Locate and identify every blood parasite.
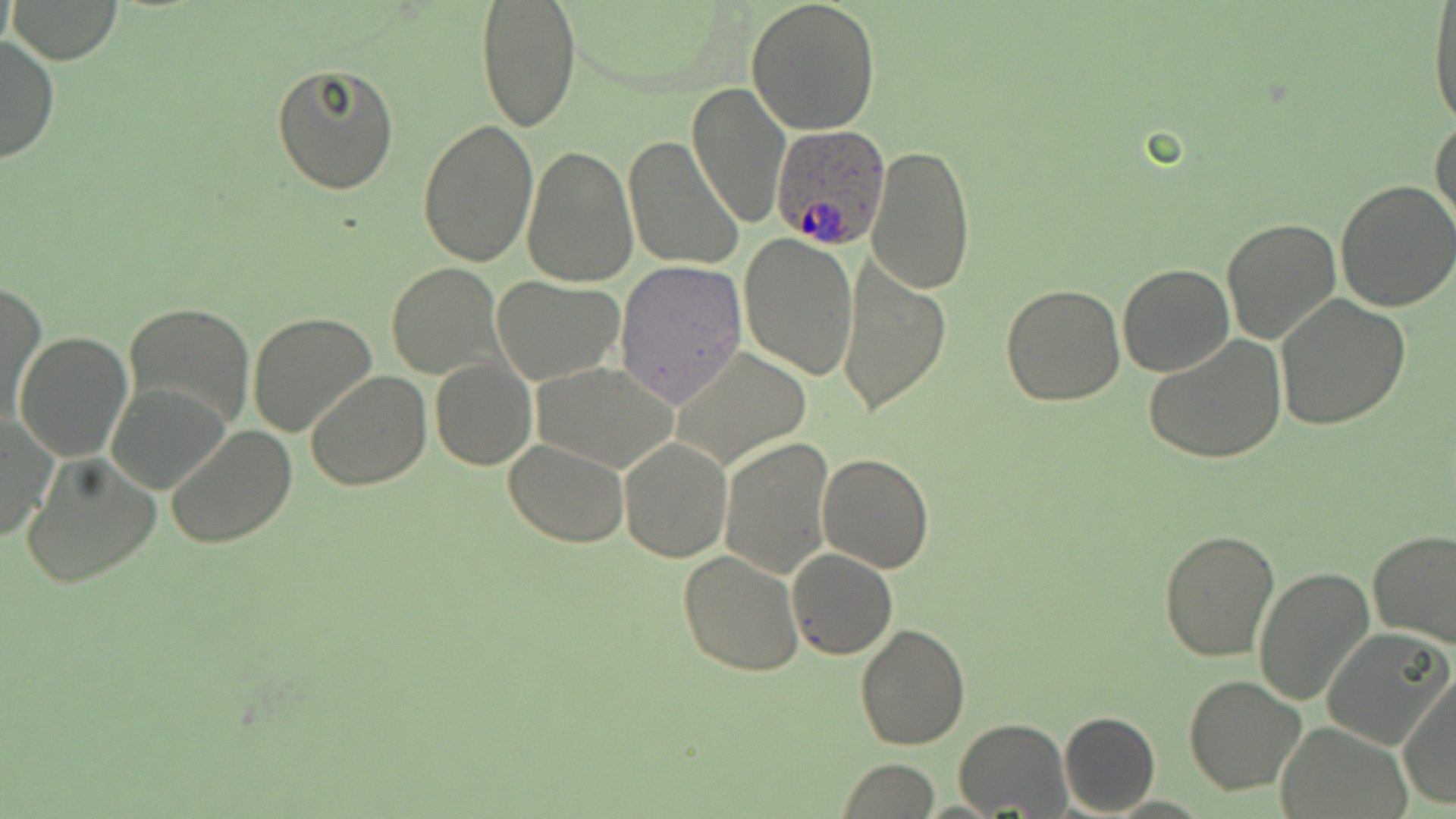

Approximate bounding boxes as [x1, y1, x2, y2] in pixels.
Plasmodium ovale-infected red blood cells: [772, 122, 889, 249].
No Plasmodium falciparum, Plasmodium malariae, Plasmodium vivax, Babesia divergens, or Trypanosoma brucei observed.

Summary:
  - Uninfected red blood cell locations: [7, 0, 124, 65], [475, 0, 581, 133], [746, 1, 883, 137], [1426, 6, 1456, 133], [0, 33, 58, 165], [271, 62, 399, 195], [687, 84, 788, 230], [1430, 116, 1455, 237], [416, 119, 539, 267], [623, 137, 744, 272], [519, 143, 638, 288], [866, 143, 976, 296], [1334, 178, 1456, 314], [1222, 214, 1343, 346], [737, 232, 858, 381], [837, 255, 952, 420], [615, 260, 747, 408], [387, 263, 503, 379], [1117, 264, 1233, 377], [493, 276, 622, 384], [2, 281, 46, 425], [1002, 283, 1128, 406], [1275, 296, 1409, 430], [122, 302, 256, 431], [247, 312, 378, 436], [15, 331, 132, 463], [1143, 336, 1287, 465], [670, 346, 814, 470], [429, 358, 536, 472], [531, 363, 680, 472], [305, 371, 432, 491], [107, 380, 232, 493], [0, 414, 55, 545], [165, 425, 297, 550], [720, 436, 834, 578], [619, 438, 731, 563], [505, 439, 631, 547], [20, 453, 162, 589], [818, 453, 935, 573], [1158, 528, 1283, 663], [1368, 531, 1456, 647], [788, 548, 896, 659], [679, 551, 804, 677], [1254, 564, 1376, 707], [857, 621, 971, 750], [1321, 628, 1452, 750], [1184, 673, 1308, 795], [1398, 674, 1455, 808], [1059, 711, 1161, 816], [955, 718, 1070, 817], [1275, 721, 1407, 817], [837, 758, 939, 818]
  - Slide-level diagnosis: Plasmodium ovale
  - Magnification: 1000x
  - Modality: light microscopy
  - Preparation: thin blood smear
  - Stain: May-Grünwald-Giemsa
  - Image size: 1456×819 pixels
  - Field of view: one of a larger specimen